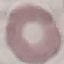
Summary:
  - Result: negative for malaria parasites
  - Preparation: thin blood smear
  - Image type: cell patch, automatically extracted from a larger field of view and resized to 64 × 64 pixels
  - Stain: Giemsa
  - Capture: smartphone through the microscope eyepiece